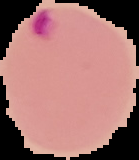
Malaria status: parasitized. Cell region segmented out of the field of view; the surrounding area is masked to black. From a thin blood film. Image is 139×160 pixels.